Locate and identify every blood parasite.
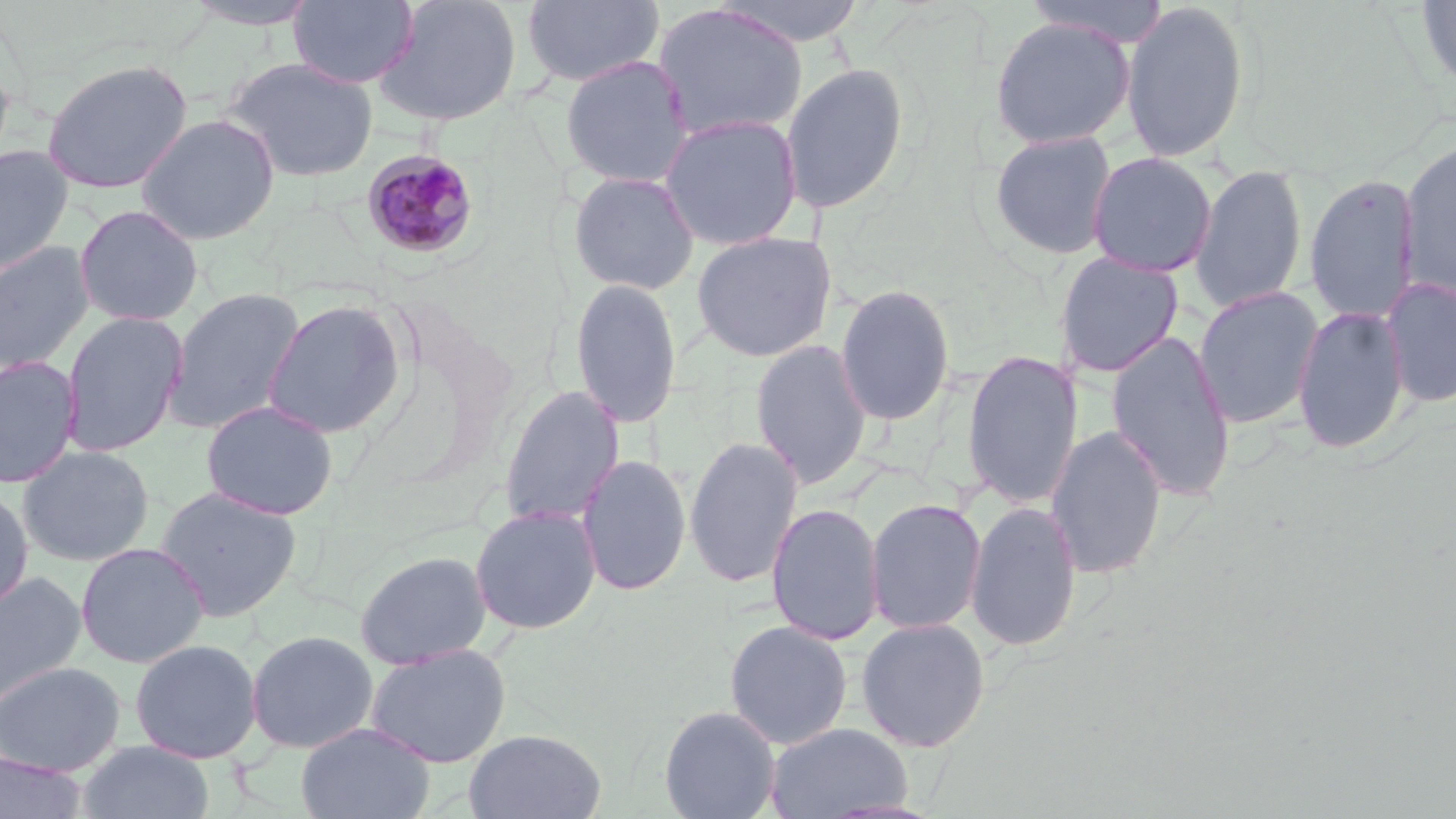

Approximate bounding boxes as named x1/y1/x2/y2 corners in pixels.
Plasmodium malariae-infected red blood cells: (x1=360, y1=148, x2=482, y2=260).
No Plasmodium falciparum, Plasmodium ovale, Plasmodium vivax, Babesia divergens, or Trypanosoma brucei observed.

slide-level diagnosis = Plasmodium malariae
preparation = thin blood film
modality = optical microscopy
image size = 1456×819 pixels
field of view = single
uninfected red blood cell locations = approximate bounding boxes as named x1/y1/x2/y2 corners in pixels: (x1=288, y1=0, x2=419, y2=88), (x1=373, y1=0, x2=523, y2=128), (x1=521, y1=0, x2=665, y2=88), (x1=708, y1=0, x2=870, y2=46), (x1=1417, y1=0, x2=1456, y2=92), (x1=181, y1=1, x2=322, y2=30), (x1=1024, y1=1, x2=1168, y2=47), (x1=1120, y1=1, x2=1250, y2=163), (x1=652, y1=3, x2=808, y2=143), (x1=988, y1=16, x2=1136, y2=149), (x1=0, y1=47, x2=16, y2=177), (x1=560, y1=55, x2=694, y2=189), (x1=219, y1=56, x2=378, y2=182), (x1=41, y1=58, x2=193, y2=194), (x1=780, y1=62, x2=909, y2=214), (x1=135, y1=113, x2=280, y2=245), (x1=659, y1=113, x2=803, y2=251), (x1=987, y1=129, x2=1118, y2=260), (x1=1398, y1=137, x2=1456, y2=304), (x1=0, y1=144, x2=74, y2=278), (x1=1087, y1=152, x2=1218, y2=277), (x1=1190, y1=164, x2=1308, y2=314), (x1=568, y1=171, x2=700, y2=295), (x1=1304, y1=173, x2=1421, y2=324), (x1=73, y1=204, x2=203, y2=326), (x1=692, y1=231, x2=836, y2=362), (x1=0, y1=241, x2=96, y2=375), (x1=1054, y1=252, x2=1184, y2=377), (x1=1381, y1=276, x2=1455, y2=409), (x1=569, y1=277, x2=683, y2=428), (x1=835, y1=283, x2=955, y2=426), (x1=1193, y1=285, x2=1323, y2=428), (x1=164, y1=287, x2=306, y2=434), (x1=261, y1=298, x2=408, y2=439), (x1=1292, y1=304, x2=1409, y2=454), (x1=59, y1=310, x2=188, y2=458), (x1=1105, y1=329, x2=1236, y2=501), (x1=751, y1=338, x2=872, y2=489), (x1=961, y1=350, x2=1084, y2=510), (x1=0, y1=355, x2=82, y2=489), (x1=498, y1=385, x2=624, y2=528), (x1=200, y1=399, x2=338, y2=520), (x1=1046, y1=425, x2=1167, y2=580), (x1=684, y1=436, x2=803, y2=589), (x1=17, y1=445, x2=154, y2=566), (x1=577, y1=453, x2=691, y2=596), (x1=154, y1=484, x2=303, y2=622), (x1=0, y1=485, x2=34, y2=615), (x1=865, y1=497, x2=987, y2=635), (x1=965, y1=501, x2=1082, y2=653), (x1=766, y1=502, x2=885, y2=645), (x1=470, y1=504, x2=601, y2=635), (x1=75, y1=541, x2=210, y2=668), (x1=354, y1=549, x2=492, y2=669), (x1=0, y1=570, x2=88, y2=709), (x1=855, y1=617, x2=991, y2=752), (x1=724, y1=620, x2=853, y2=749), (x1=245, y1=629, x2=379, y2=753), (x1=129, y1=638, x2=263, y2=763), (x1=364, y1=643, x2=512, y2=768), (x1=0, y1=661, x2=125, y2=776), (x1=659, y1=705, x2=781, y2=819), (x1=296, y1=722, x2=435, y2=819), (x1=765, y1=722, x2=914, y2=818), (x1=465, y1=729, x2=607, y2=818), (x1=77, y1=740, x2=215, y2=819), (x1=0, y1=752, x2=88, y2=819)
magnification = 1000x
stain = May-Grünwald-Giemsa